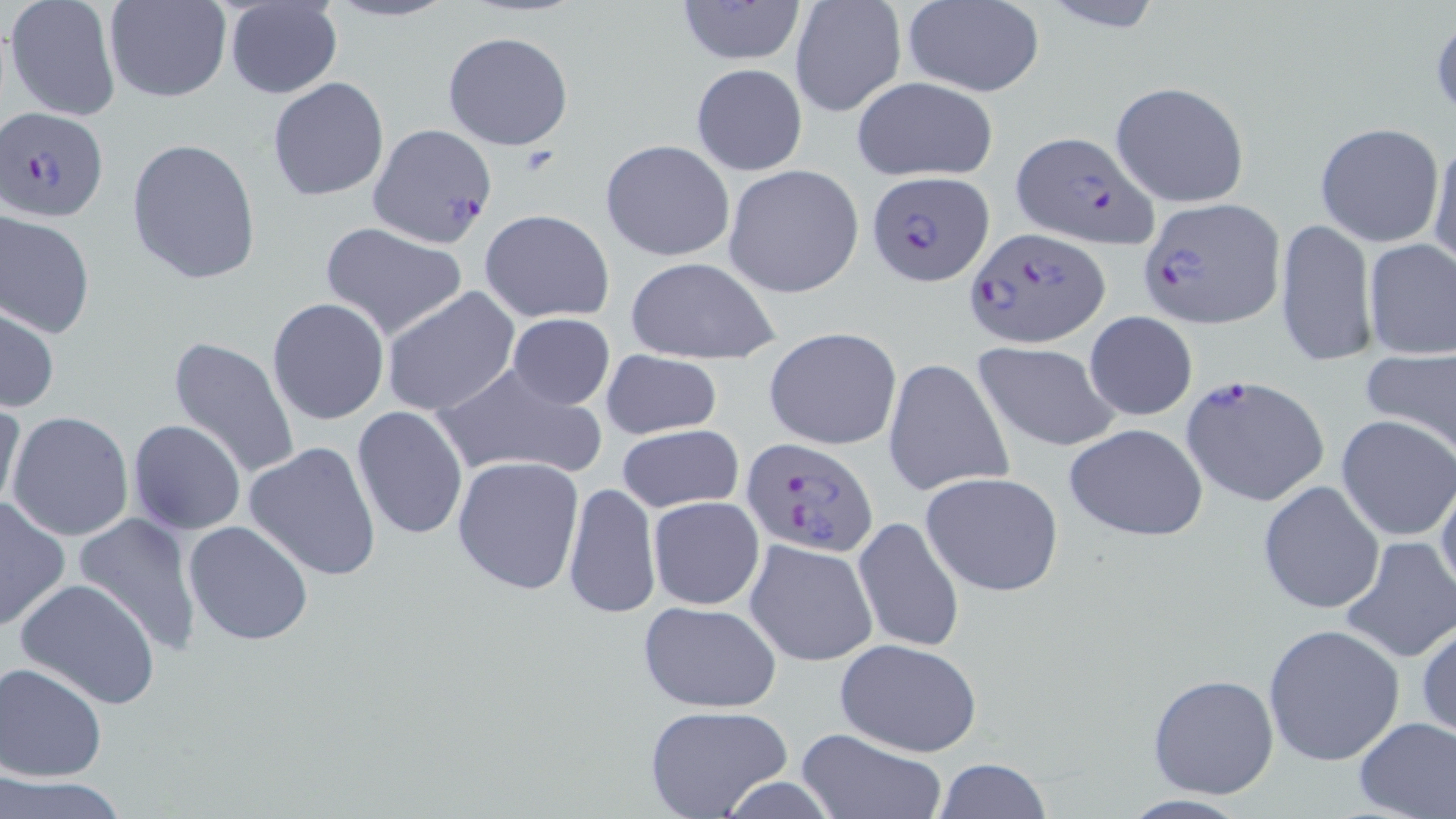
Summary:
  - Coordinate format: approximate bounding boxes as (x1, y1, x2, y2) in pixels
  - Plasmodium falciparum-infected red blood cell locations: (1, 106, 109, 224), (367, 122, 497, 250), (1010, 129, 1157, 249), (869, 170, 994, 286), (1139, 198, 1284, 328), (967, 227, 1109, 349), (1181, 375, 1330, 506), (742, 437, 877, 557)
  - Uninfected red blood cell locations: (224, 0, 343, 99), (322, 0, 458, 24), (676, 0, 807, 65), (901, 0, 1045, 96), (4, 1, 122, 122), (103, 1, 232, 104), (789, 1, 906, 119), (1039, 2, 1169, 34), (443, 30, 575, 152), (689, 63, 807, 175), (267, 76, 389, 202), (851, 76, 1000, 184), (1109, 81, 1250, 207), (1314, 122, 1445, 249), (1428, 133, 1456, 271), (126, 138, 260, 285), (599, 138, 735, 263), (723, 164, 864, 299), (1, 209, 96, 339), (478, 210, 614, 322), (1274, 217, 1376, 370), (320, 222, 468, 342), (1362, 238, 1456, 359), (625, 256, 780, 363), (381, 287, 519, 417), (267, 297, 390, 426), (2, 303, 59, 415), (1083, 311, 1198, 421), (503, 312, 617, 410), (764, 328, 902, 452), (169, 336, 301, 480), (972, 343, 1119, 452), (1359, 345, 1456, 457), (600, 349, 721, 440), (883, 358, 1014, 498), (432, 363, 604, 482), (0, 400, 25, 518), (351, 406, 468, 540), (6, 410, 135, 542), (1337, 415, 1456, 542), (128, 419, 247, 536), (1063, 421, 1209, 542), (616, 423, 744, 513), (244, 440, 384, 581), (451, 455, 586, 596), (1434, 471, 1456, 600), (919, 472, 1064, 595), (1257, 480, 1384, 615), (563, 481, 659, 617), (0, 495, 71, 633), (648, 496, 764, 609), (74, 512, 204, 656), (851, 516, 965, 654), (182, 520, 314, 647), (1338, 535, 1455, 663), (744, 537, 878, 668), (14, 578, 161, 708), (639, 601, 784, 712), (1416, 619, 1456, 743), (1261, 622, 1407, 766), (833, 637, 982, 757), (0, 662, 107, 783), (1147, 673, 1280, 800), (645, 705, 792, 818), (1352, 716, 1456, 819), (791, 727, 945, 819), (933, 758, 1053, 818), (0, 775, 131, 818)
  - Slide-level diagnosis: Plasmodium falciparum
  - Modality: light microscopy
  - Magnification: 1000x
  - Stain: May-Grünwald-Giemsa
  - Preparation: thin blood film
  - Field of view: one of a larger specimen
  - Image size: 1456×819 pixels